State which parasite is depicted.
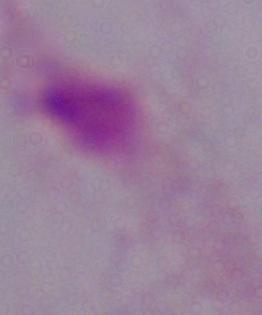

This is a trichomonad.

Summary:
  - Modality: micrograph
  - Magnification: 1000x